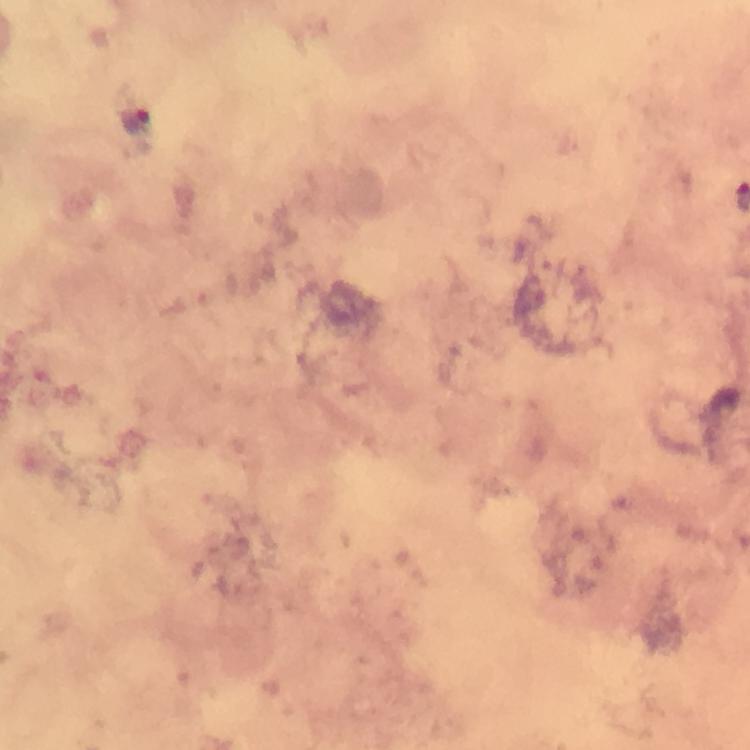

Approximate object centers, in pixels from the top-left corner.
Summary:
  - Malaria parasite locations: (x=137, y=119)
  - Cropped from: one field of view
  - Magnification: 100x
  - Immersion oil: used
  - Context: from a diagnostic examination for malaria
  - Image size: 750×750 pixels
  - Stain: Giemsa
  - Preparation: thick blood smear
  - Capture: smartphone mounted on the microscope